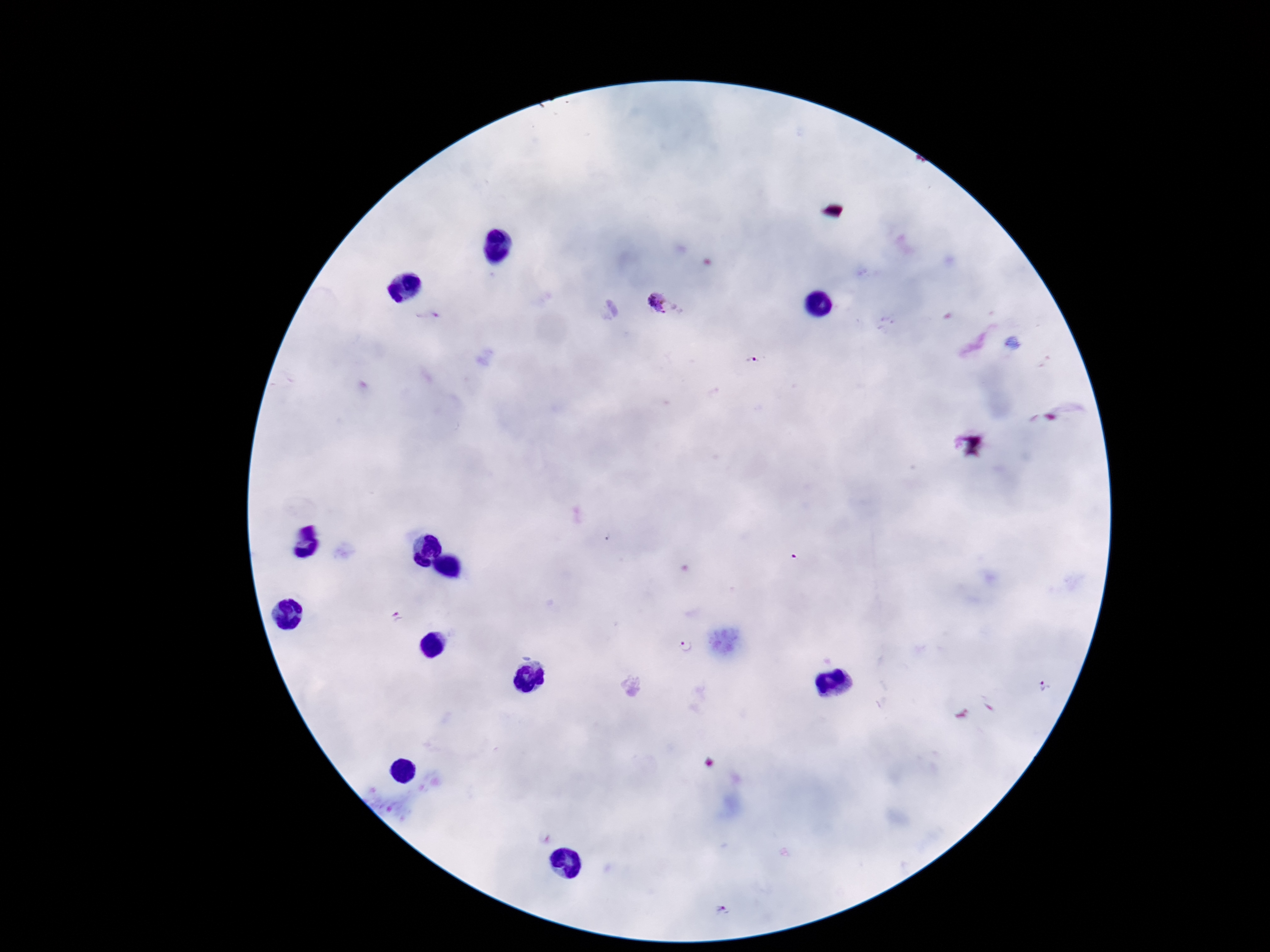

Approximate centers as [x, y] in pixels.
Summary:
  - Plasmodium parasite locations: [660, 303], [755, 360], [683, 645], [1046, 686]
  - Image size: 1270×952 pixels
  - Magnification: 100x
  - Preparation: thick blood film
  - Capture: smartphone camera through the microscope eyepiece
  - Field of view: one from this slide
  - Patient malaria status: positive
  - Stain: Giemsa